Classify this cell by malaria status.
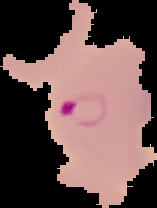

Parasitized.

image_size: 157×208 pixels
preparation: thin blood smear
image_type: segmented cell region on a black background